Report the malaria status of this cell.
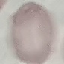
It is uninfected.

Giemsa-stained preparation. Cell patch, automatically extracted from a larger field of view and resized to 64 × 64 pixels. Thin smear of blood. Photographed with a smartphone camera at the microscope eyepiece.